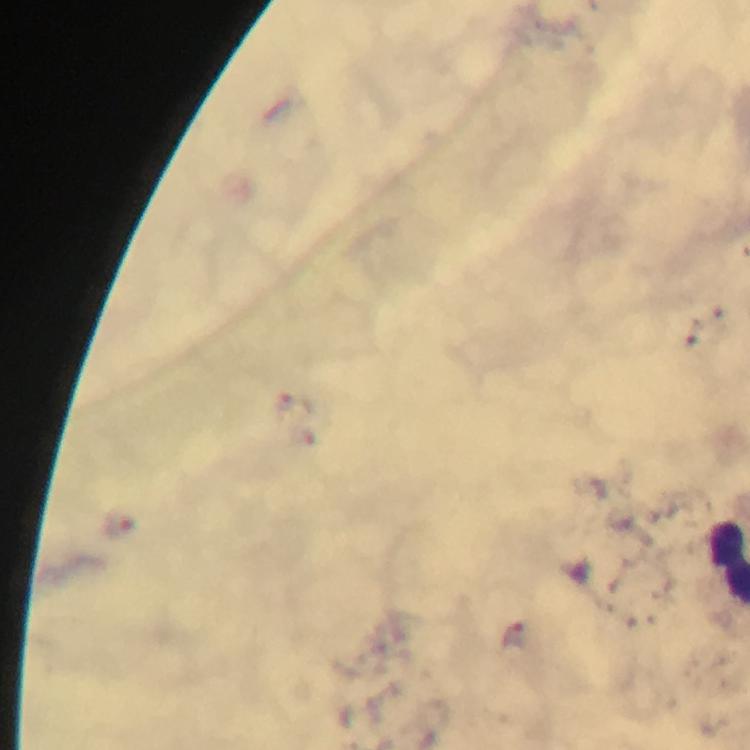
Approximate centers as [x, y] in pixels. Plasmodium parasite locations: [120, 524], [514, 635]. 100x magnification. Image is 750×750 pixels. A crop from one field of view. Thick smear. Giemsa-stained preparation. From a diagnostic examination for malaria. Immersion oil was used. Photographed through the microscope with a smartphone camera.